State the blood parasite species.
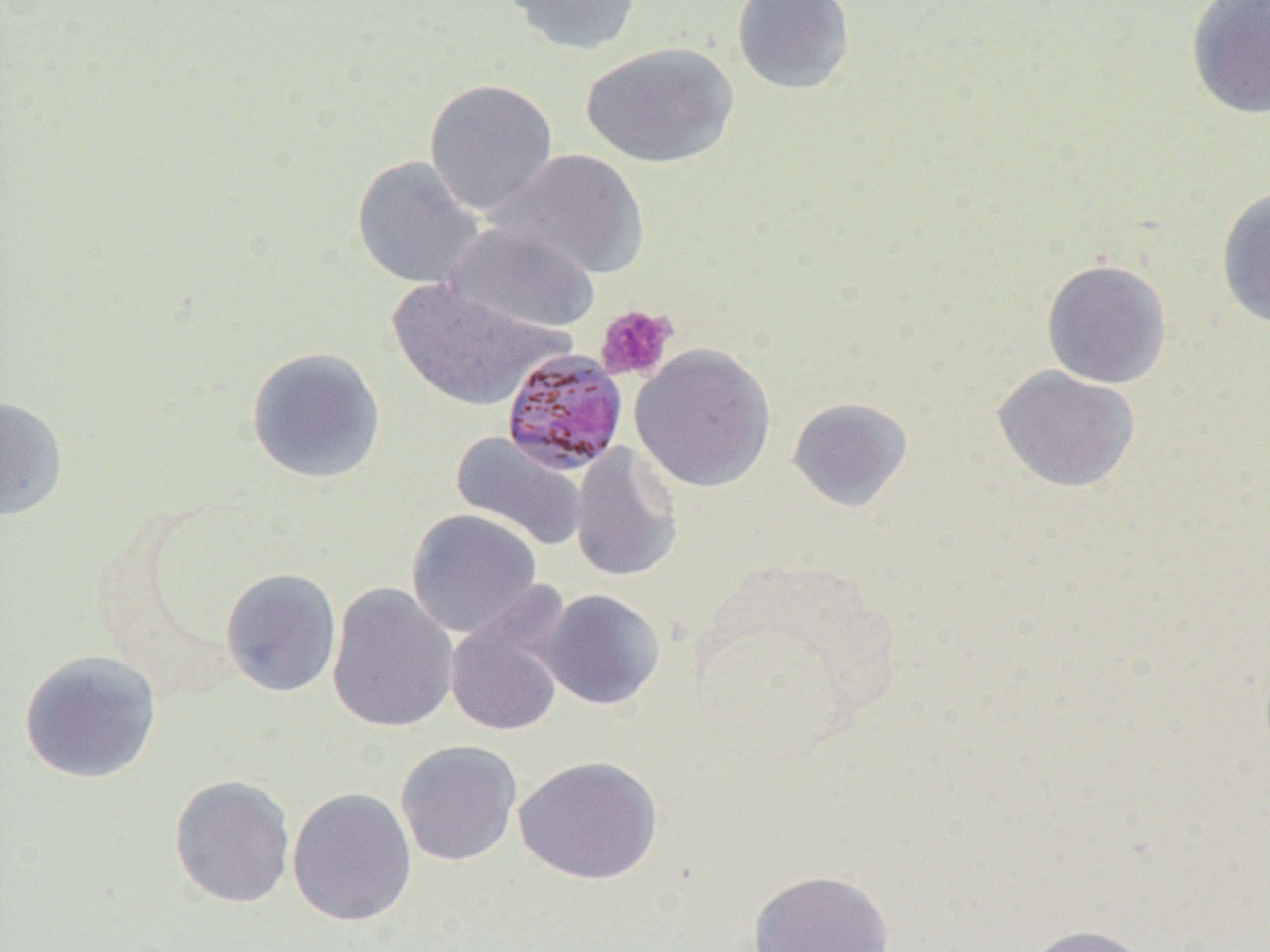
Plasmodium malariae.

Approximate bounding boxes as named x1/y1/x2/y2 corners in pixels. Platelet locations: (x1=594, y1=304, x2=677, y2=381). Plasmodium malariae-infected red blood cell locations: (x1=500, y1=348, x2=629, y2=475). Uninfected red blood cell locations: (x1=502, y1=0, x2=643, y2=56), (x1=731, y1=0, x2=856, y2=96), (x1=1185, y1=0, x2=1270, y2=120), (x1=580, y1=42, x2=739, y2=169), (x1=424, y1=78, x2=558, y2=218), (x1=488, y1=148, x2=650, y2=281), (x1=351, y1=154, x2=486, y2=290), (x1=1215, y1=185, x2=1270, y2=330), (x1=442, y1=222, x2=600, y2=337), (x1=1040, y1=258, x2=1172, y2=389), (x1=388, y1=277, x2=563, y2=411), (x1=630, y1=343, x2=776, y2=492), (x1=246, y1=346, x2=387, y2=484), (x1=992, y1=365, x2=1141, y2=493), (x1=0, y1=396, x2=70, y2=520), (x1=787, y1=396, x2=914, y2=512), (x1=449, y1=431, x2=590, y2=553), (x1=570, y1=442, x2=684, y2=583), (x1=406, y1=509, x2=543, y2=638), (x1=220, y1=567, x2=343, y2=698), (x1=326, y1=582, x2=459, y2=734), (x1=537, y1=588, x2=667, y2=711), (x1=443, y1=589, x2=574, y2=738), (x1=18, y1=649, x2=163, y2=785), (x1=395, y1=740, x2=522, y2=866), (x1=513, y1=755, x2=663, y2=885), (x1=168, y1=774, x2=296, y2=909), (x1=287, y1=787, x2=418, y2=926), (x1=748, y1=869, x2=895, y2=952), (x1=1023, y1=923, x2=1157, y2=952). Thin blood film. Optical microscopy. Captured at 1000x magnification. One field of a larger specimen. Image is 1270×952 pixels.